Outline each blood parasite and name the species.
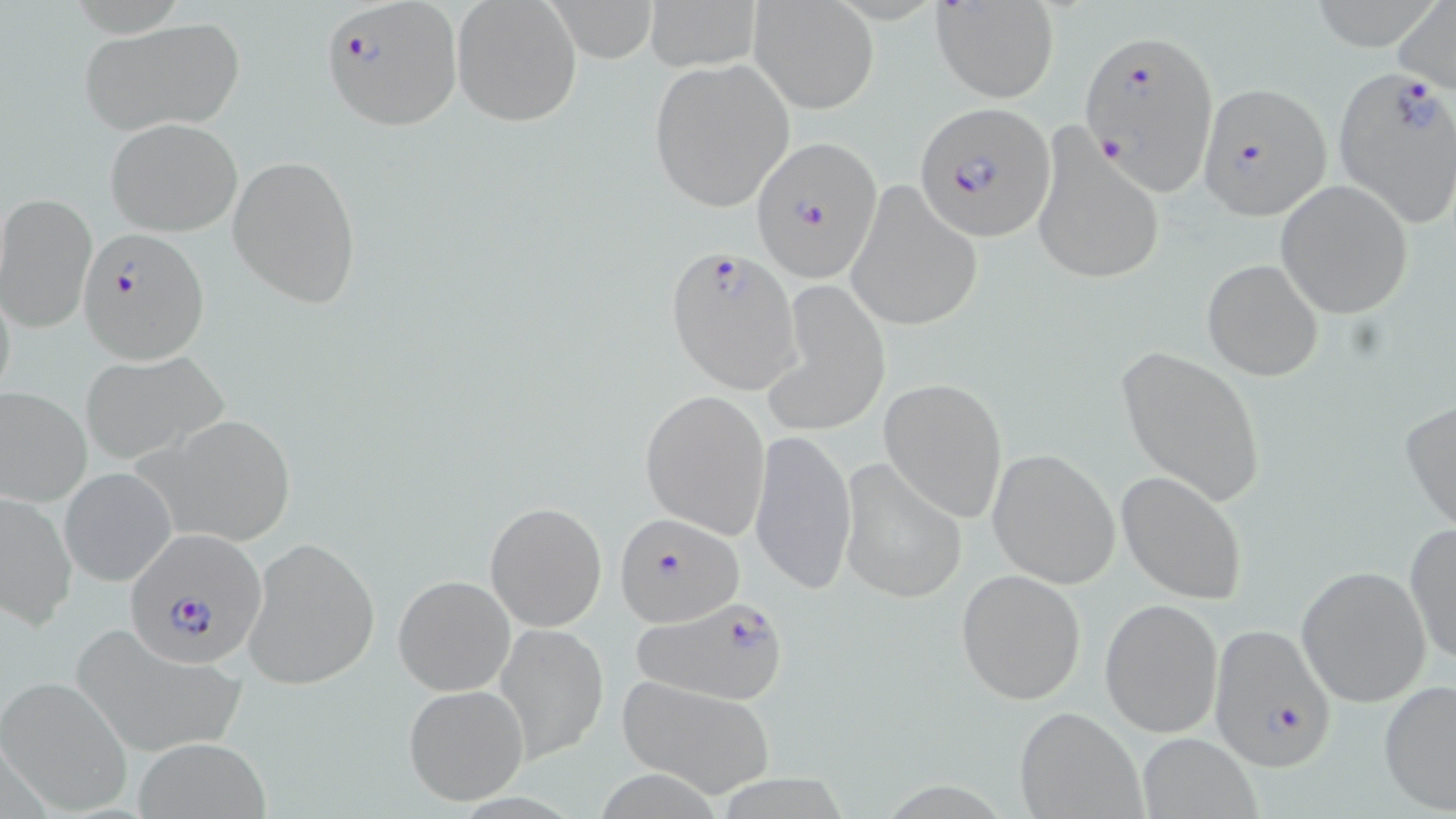

Approximate bounding boxes as (x1,y1)-(x2,y2) corner pairs in pixels.
Plasmodium falciparum-infected red blood cells: (324,1)-(462,130), (1080,29)-(1218,196), (1330,65)-(1456,227), (1196,81)-(1329,217), (915,101)-(1056,241), (753,135)-(883,284), (78,226)-(210,363), (664,246)-(804,392), (616,510)-(744,628), (128,531)-(265,665), (629,597)-(795,705), (1210,622)-(1339,774).
No Plasmodium ovale, Plasmodium malariae, Plasmodium vivax, Babesia divergens, or Trypanosoma brucei observed.

Uninfected red blood cell locations: (451,0)-(582,127), (545,0)-(661,59), (645,0)-(762,72), (1393,0)-(1456,95), (931,1)-(1060,103), (749,2)-(877,114), (79,20)-(243,136), (647,59)-(795,213), (104,118)-(241,237), (1031,128)-(1165,287), (228,155)-(362,307), (848,180)-(983,333), (1275,180)-(1414,319), (0,192)-(96,333), (1202,258)-(1325,382), (763,281)-(891,438), (1115,344)-(1266,507), (79,351)-(230,467), (879,378)-(1007,522), (0,386)-(92,506), (640,389)-(771,540), (1400,397)-(1456,534), (133,413)-(296,547), (750,428)-(857,596), (987,447)-(1121,589), (837,459)-(967,604), (60,467)-(177,587), (1117,472)-(1250,605), (0,491)-(75,630), (485,500)-(607,631), (1403,522)-(1456,670), (243,535)-(380,688), (1296,564)-(1432,707), (956,568)-(1087,704), (393,573)-(516,696), (1099,597)-(1222,739), (497,621)-(608,761), (69,622)-(244,756), (615,674)-(777,799), (0,676)-(129,812), (1377,678)-(1456,815), (403,683)-(531,806), (1014,704)-(1147,819), (1137,732)-(1262,817), (134,739)-(269,817). Slide-level diagnosis: Plasmodium falciparum. Image is 1456×819 pixels. Captured at 1000x magnification. Thin blood film. Light microscopy. Single field of view. May-Grünwald-Giemsa stain.